Locate and identify every blood parasite.
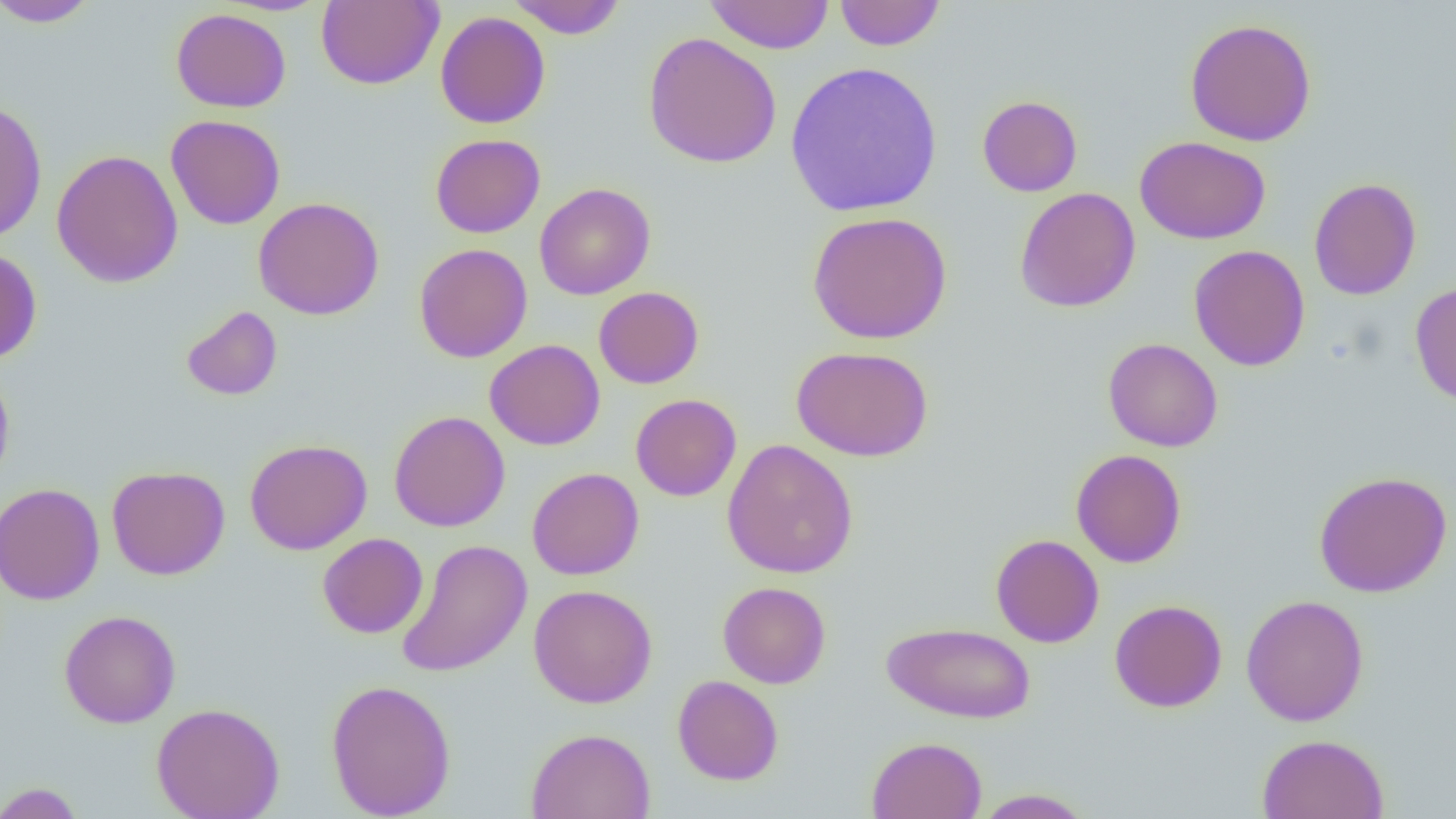
No blood parasites seen.

Summary:
  - Coordinate format: approximate bounding boxes as (x1, y1, x2, y2) in pixels
  - Uninfected red blood cell locations: (0, 0, 101, 28), (316, 0, 443, 89), (507, 0, 627, 39), (703, 0, 835, 54), (834, 0, 946, 51), (677, 2, 830, 96), (171, 7, 291, 113), (435, 11, 550, 129), (1185, 18, 1317, 146), (643, 32, 782, 169), (785, 61, 943, 218), (977, 95, 1083, 197), (0, 100, 48, 243), (166, 114, 286, 230), (430, 133, 545, 238), (1135, 136, 1271, 245), (51, 149, 184, 288), (1308, 177, 1421, 300), (535, 182, 656, 300), (1014, 187, 1141, 312), (253, 197, 384, 320), (806, 211, 952, 345), (413, 243, 532, 362), (1188, 245, 1310, 371), (0, 247, 43, 365), (1409, 282, 1456, 407), (593, 286, 704, 389), (181, 305, 283, 401), (1103, 337, 1223, 452), (485, 339, 605, 451), (792, 344, 933, 461), (0, 362, 15, 489), (631, 394, 741, 501), (389, 411, 510, 532), (245, 438, 372, 555), (721, 439, 859, 579), (1070, 449, 1187, 568), (107, 465, 230, 580), (527, 467, 644, 580), (1313, 471, 1452, 597), (0, 482, 104, 606), (317, 533, 428, 638), (991, 534, 1104, 648), (396, 539, 533, 678), (717, 581, 831, 689), (528, 584, 657, 708), (1241, 594, 1369, 726), (1109, 599, 1228, 712), (58, 609, 181, 728), (881, 621, 1037, 724), (672, 674, 784, 786), (326, 678, 456, 819), (151, 702, 284, 819), (526, 728, 655, 819), (1257, 734, 1390, 819), (866, 736, 987, 818), (0, 782, 85, 819), (972, 788, 1094, 818)
  - Slide-level diagnosis: no evidence of blood parasites
  - Preparation: thin blood smear
  - Image size: 1456×819 pixels
  - Modality: optical microscopy
  - Field of view: one of a larger specimen
  - Magnification: 1000x